Report the malaria status of this cell.
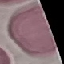

It is uninfected.

stain: Giemsa
image_type: automatically extracted cell patch, resized to 64 × 64 pixels
preparation: thin smear
capture: smartphone through the microscope eyepiece